Describe the morphology of the erythrocytes.
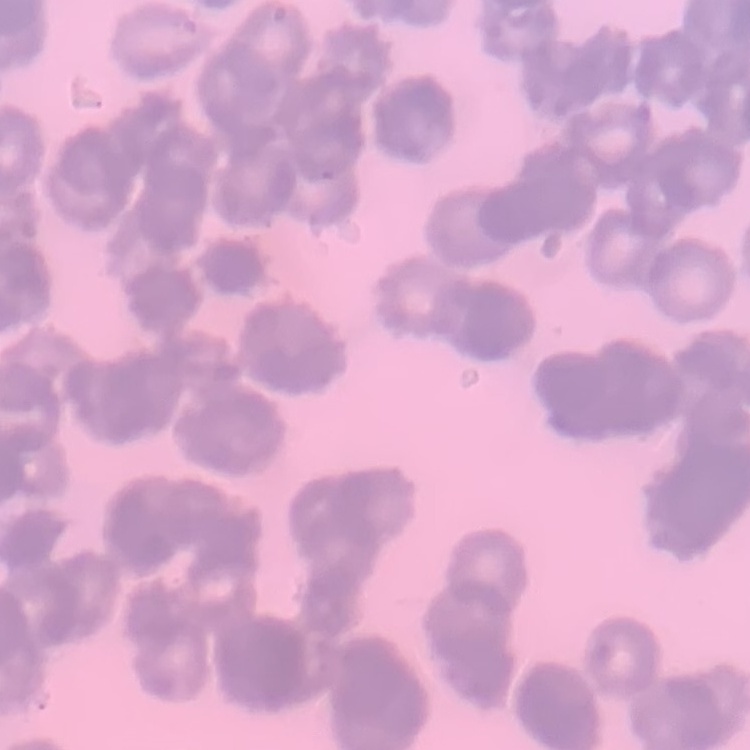

Rouleaux formation.

preparation: thin blood film
stain: Field's or Giemsa
image_type: one tile cut from a larger photomicrograph